State which cell type is depicted.
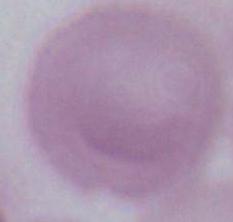

This is an erythrocyte.

Summary:
  - Magnification: 1000x
  - Modality: photomicrograph